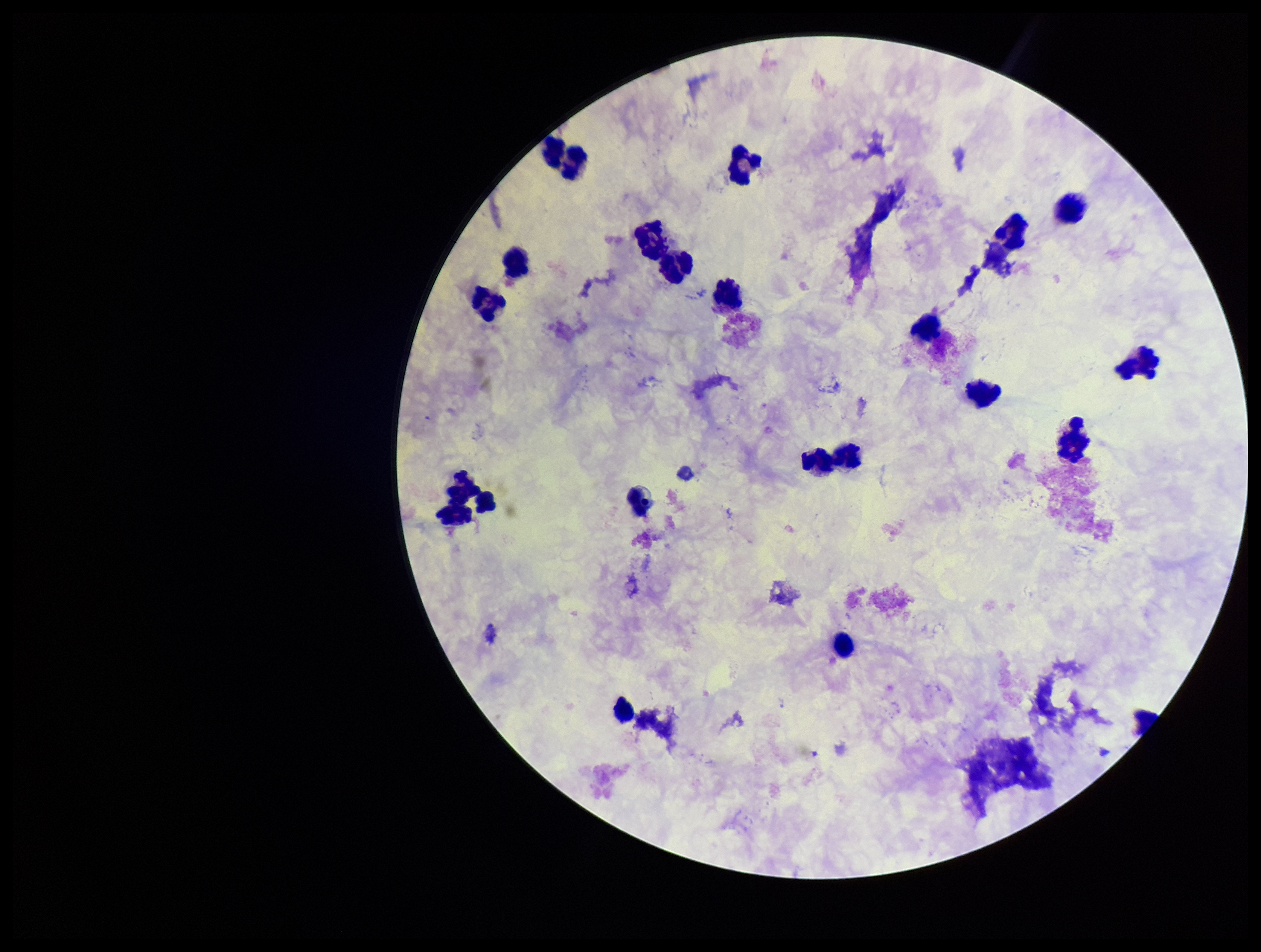

field_of_view: single
parasite_count: 0
image_size: 1261×952 pixels
patient_malaria_status: negative
stain: Giemsa
capture: smartphone photograph through the microscope eyepiece
preparation: thick blood smear
plasmodium_parasites: none detected
leukocyte_count: 19